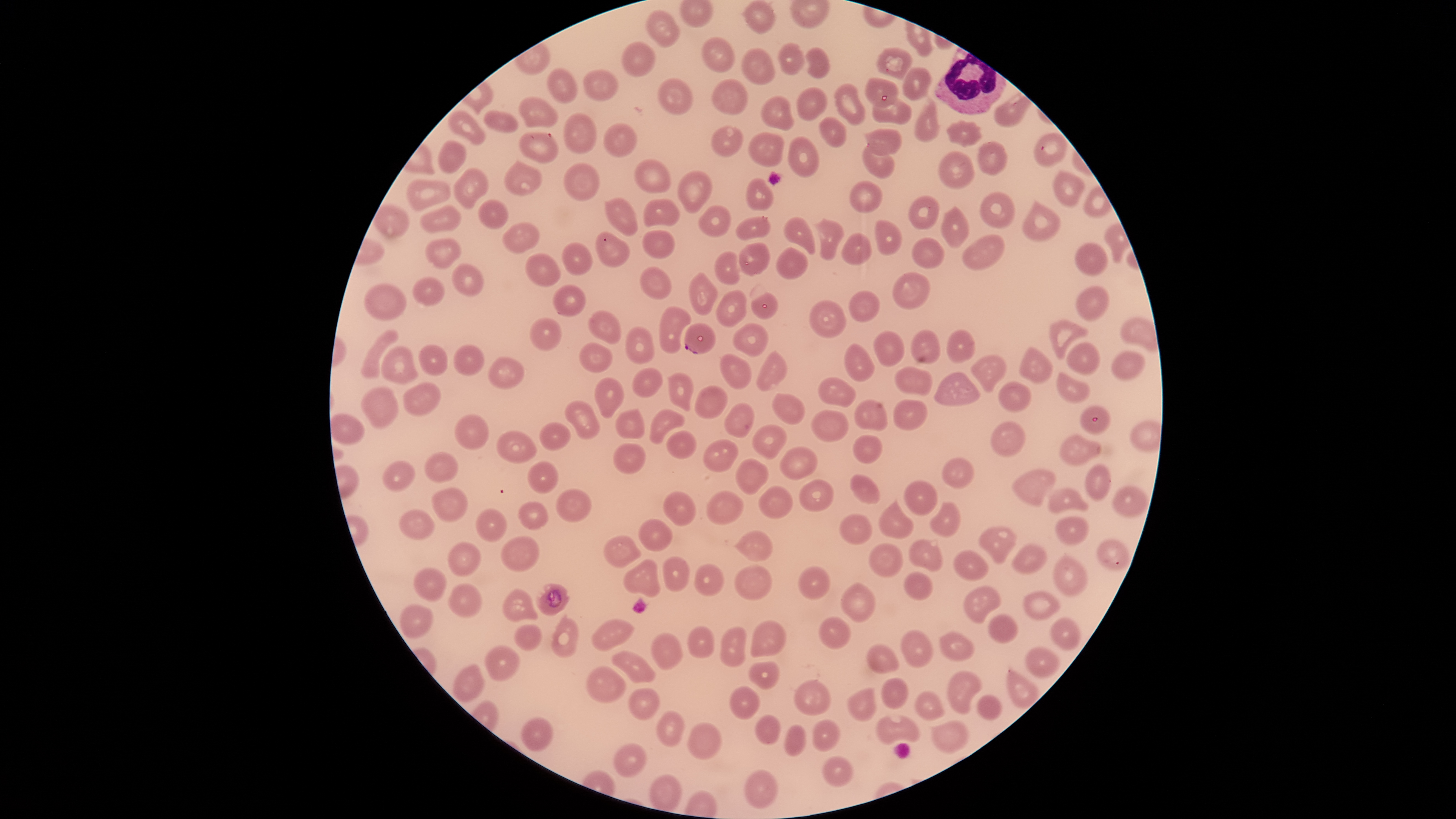
Approximate bounding boxes as {left, top, right, bottom} in pixels.
Summary:
  - WBCs: {934, 47, 1007, 115}
  - Uninfected RBCs: {741, 0, 777, 34}, {645, 9, 681, 49}, {701, 36, 734, 73}, {621, 41, 657, 77}, {777, 42, 806, 76}, {742, 47, 775, 85}, {805, 47, 830, 78}, {875, 47, 912, 80}, {901, 67, 933, 101}, {546, 68, 577, 104}, {582, 68, 619, 103}, {657, 77, 693, 116}, {710, 78, 748, 115}, {864, 78, 899, 108}, {832, 83, 867, 126}, {797, 87, 827, 122}, {760, 94, 795, 131}, {518, 96, 559, 129}, {914, 96, 941, 143}, {870, 98, 912, 126}, {447, 109, 486, 145}, {483, 109, 519, 135}, {563, 113, 597, 154}, {818, 117, 847, 148}, {945, 119, 983, 148}, {602, 122, 638, 160}, {710, 125, 743, 157}, {864, 127, 903, 157}, {518, 132, 559, 163}, {747, 132, 784, 167}, {1034, 133, 1066, 166}, {787, 136, 819, 179}, {437, 139, 468, 176}, {975, 140, 1009, 177}, {862, 147, 895, 181}, {937, 149, 975, 190}, {634, 158, 672, 194}, {503, 159, 543, 195}, {563, 162, 600, 202}, {452, 167, 489, 210}, {677, 170, 712, 214}, {1051, 170, 1085, 207}, {745, 177, 775, 211}, {407, 178, 451, 212}, {849, 181, 881, 213}, {979, 191, 1016, 229}, {907, 195, 940, 230}, {604, 197, 639, 237}, {477, 199, 510, 229}, {643, 199, 681, 227}, {1021, 199, 1062, 244}, {420, 204, 462, 234}, {697, 204, 731, 237}, {940, 204, 971, 249}, {735, 216, 771, 242}, {782, 216, 815, 255}, {814, 217, 845, 262}, {873, 219, 902, 256}, {501, 222, 540, 253}, {641, 229, 675, 260}, {595, 231, 630, 268}, {840, 232, 872, 265}, {962, 234, 1006, 271}, {911, 236, 943, 270}, {425, 237, 463, 271}, {561, 240, 594, 277}, {738, 242, 771, 277}, {1074, 242, 1109, 277}, {775, 246, 807, 280}, {713, 250, 740, 285}, {525, 253, 562, 288}, {450, 263, 484, 296}, {639, 266, 672, 300}, {688, 272, 719, 315}, {412, 275, 446, 308}, {552, 283, 586, 316}, {364, 284, 407, 321}, {1075, 285, 1112, 322}, {715, 288, 747, 327}, {848, 290, 881, 323}, {750, 291, 778, 320}, {808, 299, 846, 338}, {658, 305, 693, 354}, {587, 309, 623, 345}, {529, 318, 562, 351}, {1049, 318, 1089, 360}, {731, 322, 769, 358}, {625, 325, 656, 363}, {360, 329, 400, 379}, {873, 329, 905, 367}, {910, 329, 940, 366}, {945, 329, 974, 364}, {579, 341, 613, 373}, {843, 342, 876, 382}, {1064, 342, 1101, 377}, {418, 344, 448, 376}, {453, 344, 485, 376}, {380, 345, 419, 385}, {1018, 346, 1055, 385}, {755, 349, 789, 393}, {1111, 350, 1147, 381}, {720, 353, 753, 390}, {970, 353, 1007, 393}, {487, 356, 525, 389}, {632, 366, 664, 397}, {895, 366, 934, 397}, {1056, 371, 1090, 403}, {667, 372, 695, 411}, {933, 372, 980, 407}, {818, 376, 857, 407}, {593, 377, 624, 419}, {997, 380, 1033, 413}, {402, 381, 442, 417}, {694, 384, 729, 419}, {361, 386, 399, 430}, {771, 393, 805, 427}, {853, 399, 888, 431}, {892, 399, 929, 430}, {564, 400, 600, 440}, {723, 402, 754, 438}, {1079, 405, 1110, 435}, {614, 408, 645, 439}, {649, 408, 684, 445}, {809, 410, 849, 443}, {330, 414, 364, 446}, {454, 414, 490, 451}, {989, 421, 1027, 458}, {539, 422, 572, 452}, {752, 423, 788, 460}, {496, 430, 537, 465}, {665, 430, 697, 459}, {1058, 433, 1103, 467}, {852, 434, 884, 465}, {703, 439, 739, 473}, {612, 443, 646, 475}, {779, 446, 818, 481}, {424, 450, 459, 483}, {942, 457, 976, 489}, {735, 458, 769, 496}, {382, 460, 416, 492}, {526, 461, 559, 494}, {1084, 463, 1113, 502}, {1011, 469, 1056, 507}, {850, 474, 880, 505}, {799, 477, 835, 511}, {904, 480, 938, 516}, {1110, 484, 1149, 519}, {758, 485, 794, 520}, {1047, 485, 1089, 514}, {431, 487, 469, 523}, {556, 489, 592, 523}, {662, 490, 698, 527}, {705, 490, 746, 526}, {878, 498, 914, 541}, {517, 500, 550, 531}, {929, 501, 961, 538}, {475, 508, 508, 543}, {398, 509, 436, 540}, {839, 513, 874, 546}, {1055, 515, 1089, 547}, {637, 516, 672, 553}, {978, 526, 1018, 565}, {732, 529, 772, 562}, {499, 535, 540, 573}, {603, 535, 642, 569}, {908, 538, 944, 573}, {1095, 538, 1131, 573}, {447, 540, 482, 577}, {869, 542, 903, 578}, {1011, 544, 1048, 575}, {951, 549, 989, 582}, {1051, 554, 1089, 598}, {661, 555, 690, 592}, {623, 558, 662, 599}, {694, 562, 726, 598}, {734, 564, 772, 601}, {798, 566, 832, 601}, {413, 567, 448, 602}, {904, 571, 933, 601}, {840, 581, 877, 623}, {448, 583, 482, 618}, {964, 584, 1002, 626}, {501, 588, 538, 623}, {1023, 591, 1062, 620}, {399, 604, 434, 640}, {550, 613, 579, 659}, {987, 613, 1019, 643}, {817, 616, 851, 649}, {1049, 617, 1082, 652}, {590, 618, 636, 652}, {750, 619, 787, 657}, {514, 625, 542, 652}, {687, 625, 715, 658}, {720, 626, 748, 667}, {900, 629, 934, 667}, {940, 630, 975, 662}, {650, 632, 683, 670}, {865, 643, 900, 675}, {483, 644, 521, 682}, {1024, 647, 1061, 680}, {610, 650, 656, 684}, {747, 661, 780, 689}, {451, 664, 485, 702}, {584, 665, 628, 703}, {1006, 667, 1041, 710}, {947, 670, 983, 716}, {880, 677, 909, 709}, {794, 678, 831, 716}, {728, 684, 761, 720}, {627, 687, 662, 720}, {847, 687, 877, 722}, {914, 690, 944, 721}, {976, 695, 1003, 720}, {656, 709, 686, 747}, {875, 712, 920, 746}, {754, 713, 782, 746}, {811, 718, 841, 752}, {929, 720, 969, 753}, {687, 722, 723, 761}, {783, 724, 807, 756}, {613, 743, 648, 779}, {822, 756, 853, 788}, {744, 769, 779, 809}
  - Parasitized RBCs: {684, 323, 716, 355}, {536, 583, 571, 616}
  - Presence: malaria parasites seen
  - Capture: smartphone photograph through the microscope eyepiece
  - Species: Plasmodium falciparum
  - Image size: 1456×819 pixels
  - Visible region: circular
  - Stain: Giemsa
  - Preparation: thin blood smear
  - Field of view: single